Report the malaria status of this cell.
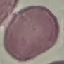
Uninfected.

Giemsa stain. Acquired by smartphone through the microscope eyepiece. Thin blood smear. Cell patch, automatically extracted from a larger field of view and resized to 64 × 64 pixels.